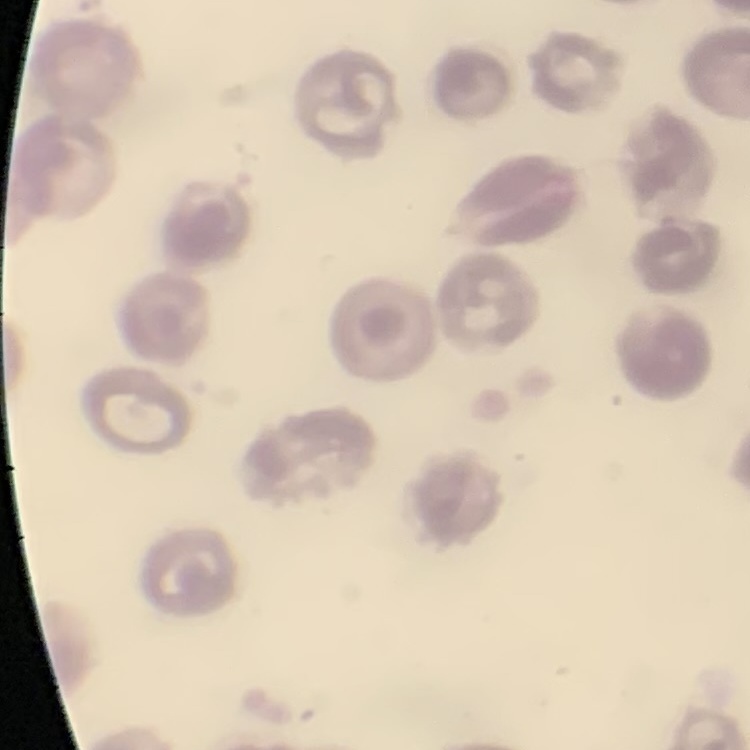 The erythrocytes exhibit no rouleaux formation. Thin blood film. Stained with either Field's or Giemsa. Square crop of a larger photomicrograph.